Classify this cell by malaria status.
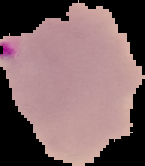
It is parasitized.

From a thin blood film. Segmented cell region on a black background. Image is 145×166 pixels.